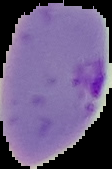
Result: Plasmodium parasites detected. Image is 112×169 pixels. Cell region segmented out of the field of view; the surrounding area is masked to black. From a thin blood smear.